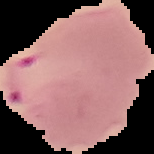
From a thin blood film. The area outside the segmented cell region is set to black. Image is 154×154 pixels. Result: malaria parasites identified.